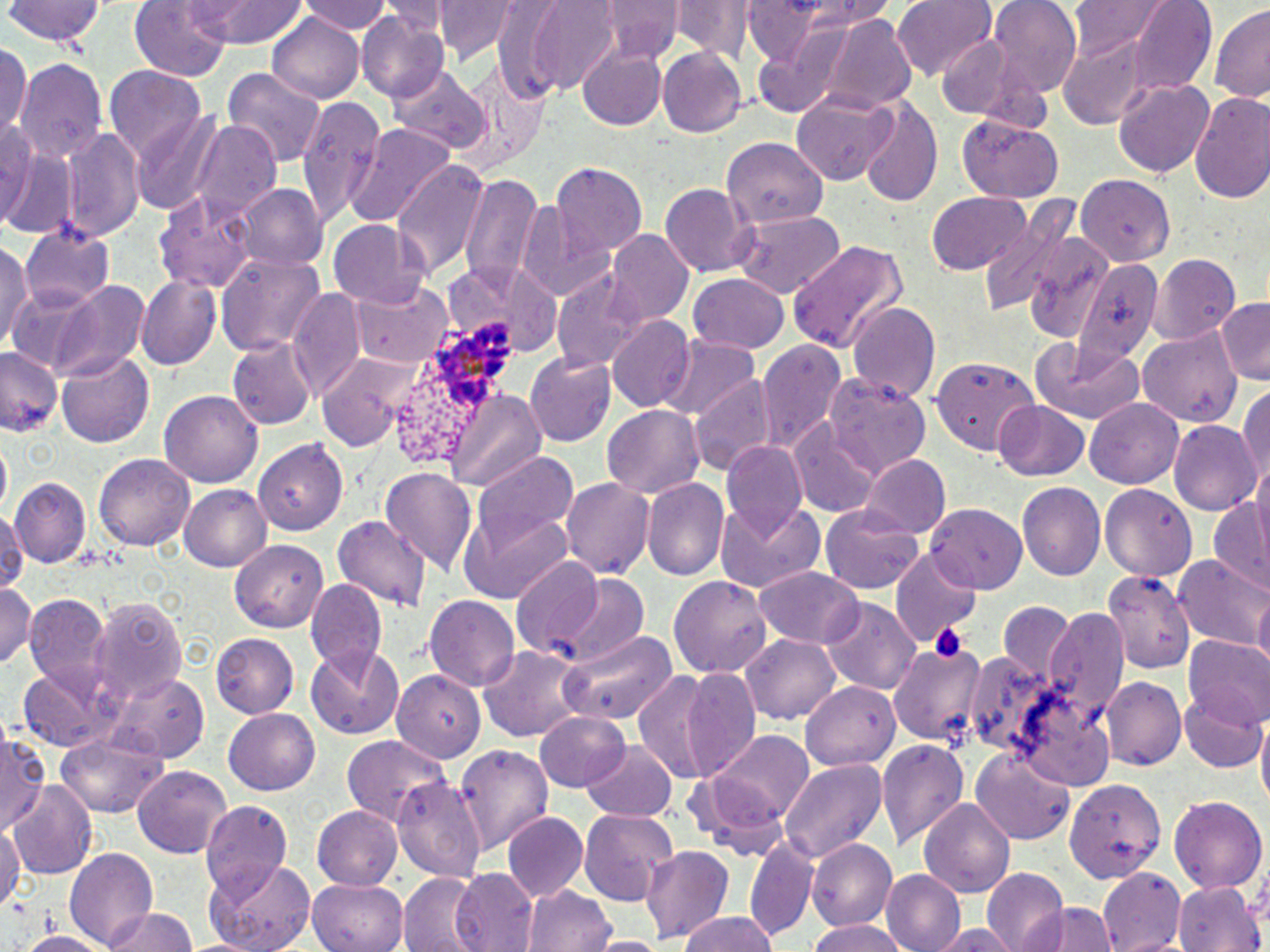

Summary:
  - Coordinate format: approximate bounding boxes as (x1,y1)-(x2,y2) corner pairs in pixels
  - Plasmodium ovale-infected red blood cell locations: (395,316)-(521,463)
  - Uninfected red blood cell locations: (5,0)-(106,49), (130,0)-(233,83), (433,0)-(522,64), (515,0)-(626,93), (592,0)-(686,65), (794,0)-(905,26), (894,0)-(997,79), (991,0)-(1084,94), (192,1)-(309,46), (303,1)-(394,38), (1066,1)-(1175,58), (1125,1)-(1218,91), (668,2)-(747,59), (1210,4)-(1270,105), (752,8)-(916,122), (357,11)-(448,103), (264,13)-(365,102), (1058,30)-(1155,125), (932,33)-(1022,120), (0,40)-(32,139), (579,44)-(666,130), (658,46)-(747,137), (15,59)-(108,171), (389,65)-(490,153), (447,65)-(549,176), (104,67)-(207,161), (222,68)-(326,166), (1113,78)-(1216,179), (790,92)-(898,185), (1189,92)-(1270,206), (297,97)-(385,226), (856,97)-(943,209), (131,112)-(225,212), (956,115)-(1064,201), (0,117)-(41,224), (188,121)-(280,224), (344,123)-(453,226), (62,129)-(147,243), (723,136)-(826,227), (2,141)-(74,237), (390,160)-(489,278), (549,164)-(646,262), (460,173)-(547,292), (1074,175)-(1173,263), (660,183)-(754,276), (237,185)-(326,272), (153,191)-(259,291), (926,192)-(1032,276), (984,195)-(1078,318), (516,197)-(619,304), (730,208)-(847,297), (327,219)-(430,307), (20,222)-(116,309), (606,231)-(692,324), (1029,235)-(1119,342), (0,237)-(31,353), (790,239)-(908,351), (215,251)-(326,361), (1153,255)-(1241,343), (1067,257)-(1165,361), (445,259)-(562,359), (553,273)-(646,374), (687,273)-(789,353), (136,276)-(222,373), (46,279)-(149,380), (355,280)-(453,369), (288,289)-(367,403), (1216,297)-(1270,383), (846,299)-(942,402), (606,317)-(694,410), (1138,331)-(1243,426), (659,336)-(759,425), (1029,338)-(1146,423), (228,339)-(316,429), (756,339)-(845,452), (0,348)-(63,436), (57,349)-(154,447), (319,352)-(426,450), (527,353)-(616,445), (930,359)-(1041,450), (691,373)-(776,475), (824,374)-(932,477), (1237,384)-(1270,485), (445,389)-(546,493), (160,390)-(263,486), (1085,398)-(1183,490), (992,399)-(1089,481), (602,405)-(703,499), (1168,421)-(1260,517), (791,424)-(881,518), (254,439)-(350,536), (723,440)-(810,538), (473,449)-(579,552), (95,453)-(192,552), (862,455)-(949,540), (379,467)-(477,573), (559,476)-(655,583), (12,479)-(91,566), (644,480)-(729,582), (1018,483)-(1104,581), (1099,483)-(1195,581), (181,484)-(273,572), (714,500)-(825,594), (822,503)-(924,594), (1207,503)-(1270,593), (925,504)-(1028,591), (0,505)-(23,597), (459,507)-(573,603), (333,512)-(432,614), (232,539)-(329,630), (892,547)-(980,650), (1174,554)-(1270,647), (511,556)-(612,657), (756,568)-(863,649), (1103,568)-(1193,674), (547,573)-(651,667), (669,575)-(771,678), (306,579)-(386,673), (1236,581)-(1269,670), (0,582)-(36,672), (1253,591)-(1270,674), (425,594)-(522,690), (93,595)-(189,708), (25,596)-(116,698), (821,599)-(918,694), (999,600)-(1080,679), (1045,609)-(1130,720), (560,629)-(674,729), (210,632)-(298,716), (741,635)-(843,724), (887,636)-(989,749), (1185,638)-(1270,729), (307,644)-(406,740), (478,645)-(588,743), (19,665)-(122,751), (681,666)-(764,781), (397,671)-(485,763), (631,671)-(723,785), (105,674)-(209,762), (1103,676)-(1187,770), (802,681)-(901,770), (1181,691)-(1267,774), (1018,695)-(1119,791), (224,707)-(320,794), (536,710)-(632,791), (1257,718)-(1270,822), (0,726)-(47,833), (709,729)-(815,826), (342,734)-(451,828), (56,736)-(167,817), (877,738)-(969,850), (581,739)-(677,820), (453,742)-(554,854), (970,747)-(1076,846), (779,757)-(885,865), (133,766)-(231,859), (683,770)-(789,861), (1062,778)-(1170,886), (393,779)-(484,880), (9,783)-(97,879), (1170,794)-(1267,894), (919,798)-(1017,897), (200,802)-(293,900), (312,804)-(404,888), (579,807)-(678,904), (502,811)-(589,900), (0,819)-(21,919), (746,835)-(815,943), (807,839)-(896,931), (641,842)-(735,942), (67,846)-(160,951), (204,858)-(318,952), (1097,868)-(1187,950), (453,869)-(539,952), (884,870)-(967,952), (981,870)-(1072,952), (399,873)-(482,952), (309,876)-(407,951), (1175,881)-(1262,952), (524,883)-(615,952), (1025,900)-(1118,952), (102,907)-(201,952), (678,912)-(781,952), (805,920)-(912,952), (936,925)-(1018,951), (14,929)-(120,952), (588,937)-(666,952)
  - Slide-level diagnosis: Plasmodium ovale
  - Modality: light microscopy
  - Magnification: 1000x
  - Preparation: thin blood smear
  - Field of view: single
  - Stain: May-Grünwald-Giemsa
  - Image size: 1270×952 pixels